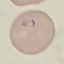
result = malaria parasites detected
capture = smartphone camera at the microscope eyepiece
image type = automatically extracted cell patch, resized to 64 × 64 pixels
preparation = thin blood film
stain = Giemsa